Assess this cell for malaria.
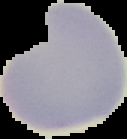
It is uninfected.

Summary:
  - Preparation: thin blood smear
  - Image type: segmented cell region on a black background
  - Image size: 127×139 pixels